Assess this cell for malaria.
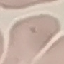
Uninfected.

{
  "capture": "smartphone through the microscope eyepiece",
  "stain": "Giemsa",
  "preparation": "thin blood film",
  "image_type": "cell patch, automatically extracted from a larger field of view and resized to 64 × 64 pixels"
}